Comment on the morphology of the erythrocytes.
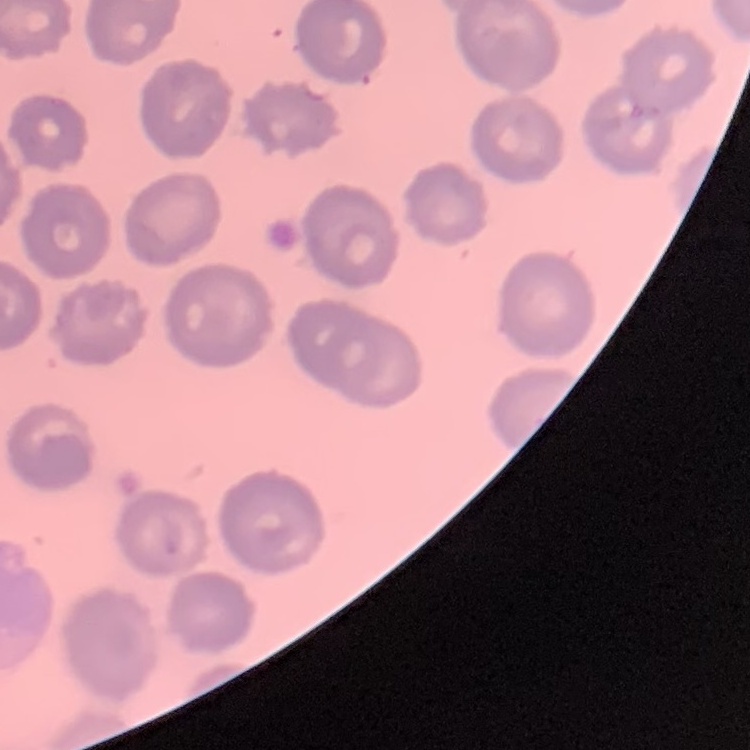

They show no rouleaux formation.

Summary:
  - Preparation: thin blood smear
  - Image type: one tile cut from a larger photomicrograph
  - Stain: Field's or Giemsa